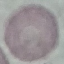
Result: no malaria parasites detected. Automatically extracted cell patch, resized to 64 × 64 pixels. Photographed with a smartphone camera at the microscope eyepiece. Thin blood smear. Giemsa-stained preparation.